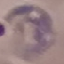
Result: malaria parasites detected. Thin blood film. Cell patch, automatically extracted from a larger field of view and resized to 64 × 64 pixels. Giemsa-stained preparation. Acquired by smartphone through the microscope eyepiece.